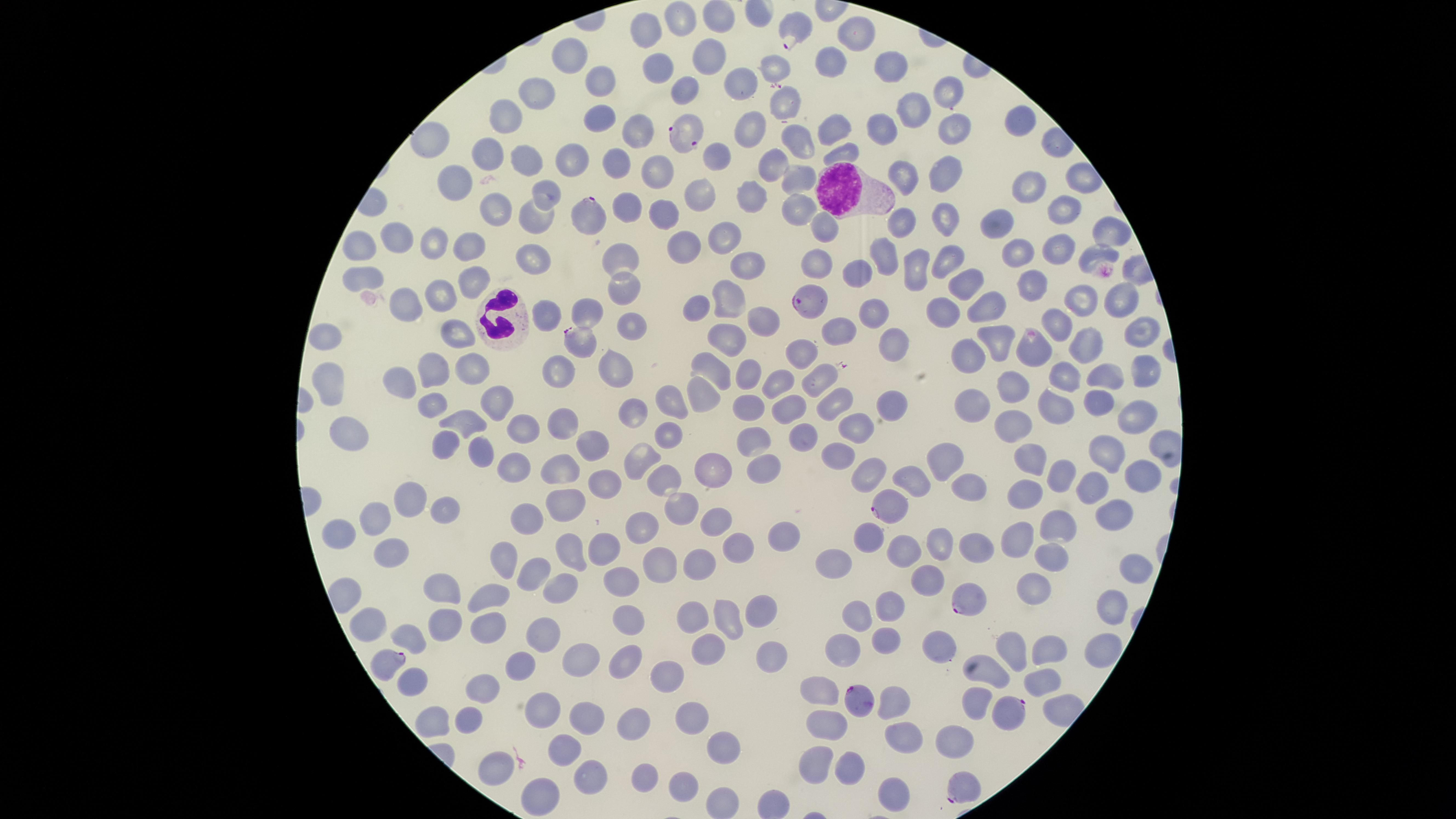

{
  "stain": "Giemsa",
  "preparation": "thin smear of blood",
  "species": "Plasmodium falciparum",
  "presence": "malaria parasites seen",
  "capture": "smartphone photograph through the microscope eyepiece",
  "uninfected_RBCs": "approximate marker points as (x, y) in pixels: (678, 21), (718, 21), (850, 27), (646, 30), (572, 55), (707, 57), (830, 61), (888, 63), (776, 67), (663, 70), (600, 79), (739, 82), (542, 87), (686, 89), (945, 91), (785, 99), (922, 109), (595, 118), (506, 120), (882, 124), (1018, 124), (959, 126), (827, 127), (638, 131), (745, 132), (797, 140), (433, 143), (842, 149), (570, 155), (714, 156), (530, 157), (491, 158), (766, 160), (614, 162), (949, 165), (665, 169), (799, 171), (452, 176), (897, 177), (1030, 181), (550, 192), (702, 193), (747, 197), (795, 203), (625, 207), (664, 207), (1062, 209), (504, 211), (940, 217), (536, 218), (906, 218), (993, 221), (819, 224), (1102, 231), (726, 237), (680, 239), (400, 241), (354, 244), (467, 244), (433, 246), (1014, 246), (1052, 251), (880, 252), (1092, 252), (537, 255), (616, 258), (946, 262), (744, 265), (816, 265), (915, 267), (855, 274), (1032, 277), (363, 280), (469, 282), (962, 285), (622, 286), (1078, 293), (727, 294), (1119, 299), (438, 302), (407, 304), (695, 307), (590, 308), (942, 308), (984, 310), (875, 312), (544, 313), (766, 316), (1055, 317), (627, 325), (841, 326), (459, 331), (1138, 331), (321, 336), (729, 337), (898, 339), (1083, 342), (997, 345), (1029, 354), (806, 356), (970, 358), (470, 364), (712, 367), (748, 367), (618, 368), (439, 369), (1145, 370), (555, 372), (1061, 372), (815, 375), (1103, 375), (402, 378), (779, 379), (1014, 381), (329, 383), (665, 393), (701, 393), (490, 397), (978, 399), (1090, 399), (749, 401), (831, 402), (1047, 403), (434, 405), (788, 406), (880, 406), (1137, 410), (637, 411), (465, 415), (560, 420), (1011, 421), (341, 425), (854, 425), (525, 428), (662, 436), (801, 437), (750, 439), (591, 447), (440, 451), (478, 455), (1027, 457), (1112, 458), (834, 459), (641, 462), (943, 464), (563, 466), (713, 467), (511, 468), (1060, 472), (660, 476), (760, 476), (863, 477), (912, 479), (1092, 480), (1143, 480), (966, 484), (605, 486), (1025, 491), (408, 498), (688, 499), (447, 502), (566, 506), (712, 514), (1111, 514), (521, 517), (377, 521), (644, 525), (1054, 527), (343, 536), (869, 536), (1020, 537), (780, 539), (940, 542), (602, 543), (901, 544), (394, 545), (969, 546), (572, 547), (737, 552), (506, 555), (1049, 556), (661, 562), (704, 562), (834, 564), (533, 572), (930, 574), (625, 575), (1133, 575), (441, 586), (564, 587), (498, 590), (1037, 591), (1109, 602), (761, 608), (883, 610), (628, 615), (725, 615), (855, 616), (693, 619), (489, 623), (367, 624), (448, 626), (410, 633), (534, 638), (884, 638), (1047, 642), (708, 646), (942, 649), (1101, 649), (1013, 650), (840, 651), (586, 655), (625, 656), (768, 657), (517, 664), (994, 670), (1038, 675), (659, 679), (412, 680), (487, 687), (825, 693), (979, 697), (897, 699), (469, 713), (540, 713), (690, 714), (584, 715), (433, 718), (830, 728), (630, 730), (911, 738), (949, 739), (557, 748), (726, 749), (846, 761), (813, 762), (497, 763), (648, 776), (588, 780), (683, 783), (896, 788), (535, 792), (718, 801)",
  "parasitized_RBCs": "approximate marker points as (x, y) in pixels: (795, 32), (691, 135), (587, 215), (804, 301), (579, 342), (891, 503), (962, 595), (387, 662), (860, 700), (1006, 708), (962, 791)",
  "visible_region": "circular",
  "field_of_view": "single",
  "WBCs": "approximate marker points as (x, y) in pixels: (835, 187), (502, 318)",
  "image_size": "1456×819 pixels"
}